Assess this cell for malaria.
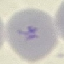
It is uninfected.

capture = smartphone through the microscope eyepiece
preparation = thin blood film
image type = cell patch, automatically extracted from a larger field of view and resized to 64 × 64 pixels
stain = Giemsa